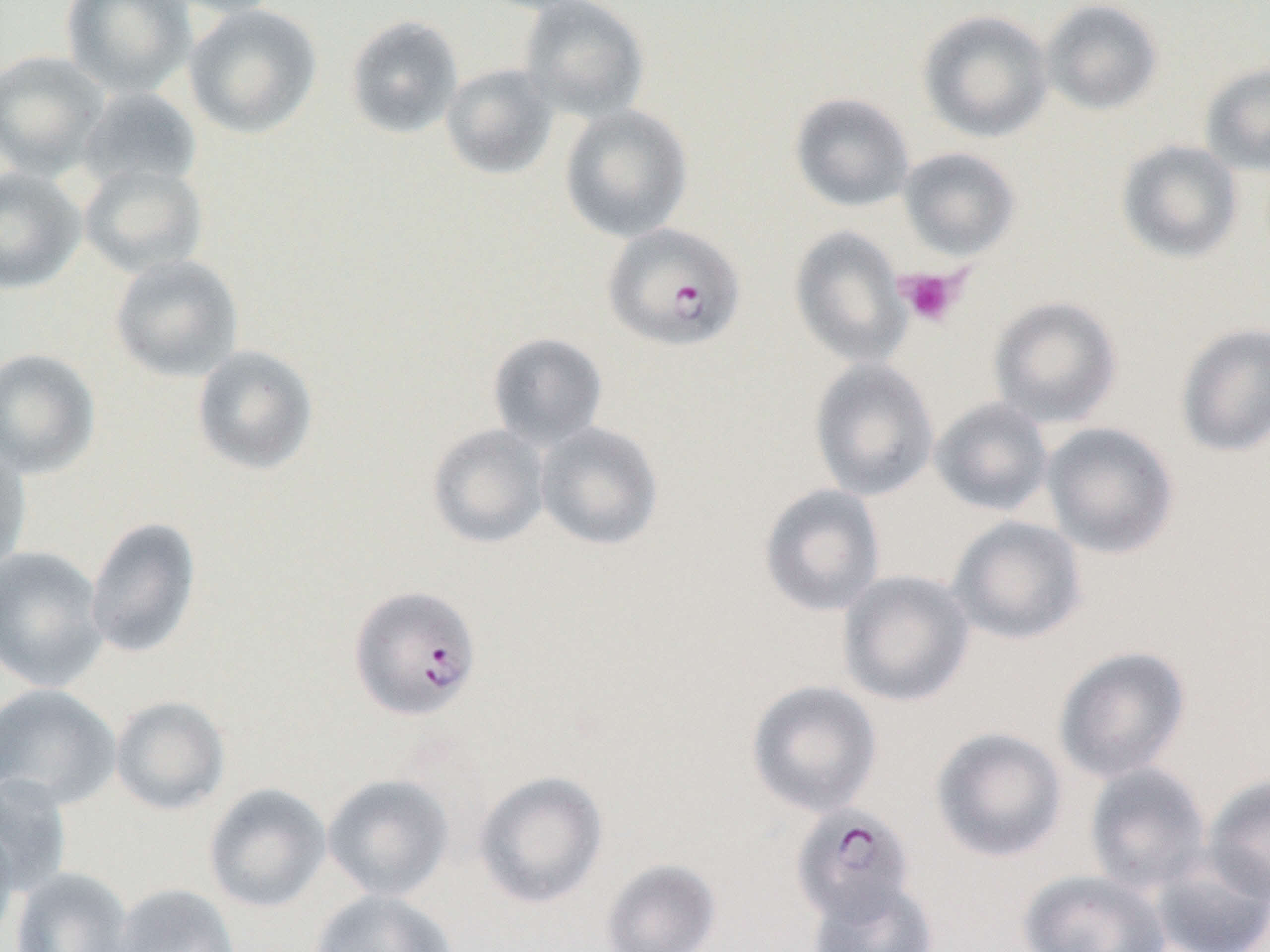
slide_level_diagnosis: Plasmodium falciparum
modality: light microscopy
magnification: 1000x
field_of_view: single
platelet_locations: 'approximate bounding boxes as [x1, y1, x2, y2] in pixels: [896, 267, 967, 327]'
uninfected_red_blood_cell_locations: 'approximate bounding boxes as [x1, y1, x2, y2] in pixels: [60, 0, 197, 98], [157, 0, 286, 18], [518, 0, 650, 122], [1041, 0, 1164, 116], [183, 4, 323, 139], [917, 9, 1053, 143], [345, 15, 464, 139], [0, 50, 110, 179], [1200, 63, 1270, 176], [441, 64, 559, 179], [78, 86, 202, 194], [789, 93, 915, 212], [559, 104, 693, 243], [1116, 139, 1244, 263], [897, 147, 1021, 261], [79, 162, 208, 278], [0, 167, 86, 294], [788, 226, 910, 367], [110, 254, 244, 382], [988, 296, 1122, 428], [1175, 323, 1270, 458], [487, 332, 609, 449], [191, 344, 319, 475], [0, 348, 101, 479], [809, 358, 940, 501], [929, 397, 1054, 517], [534, 421, 664, 551], [1041, 422, 1180, 559], [427, 423, 550, 549], [0, 442, 32, 577], [758, 483, 886, 617], [947, 515, 1088, 646], [85, 516, 202, 660], [0, 546, 108, 692], [837, 570, 975, 708], [1053, 645, 1192, 783], [746, 679, 883, 818], [0, 683, 122, 810], [110, 695, 231, 816], [930, 726, 1068, 862], [1084, 762, 1212, 895], [473, 770, 609, 909], [322, 774, 454, 902], [0, 775, 73, 896], [1203, 775, 1270, 905], [204, 783, 332, 913], [0, 822, 20, 946], [1149, 847, 1270, 952], [600, 859, 722, 952], [10, 867, 135, 952], [1019, 869, 1171, 952], [807, 878, 938, 952], [112, 883, 241, 952], [309, 889, 458, 952]'
preparation: thin blood smear
image_size: 1270×952 pixels
plasmodium_falciparum_infected_red_blood_cell_locations: 'approximate bounding boxes as [x1, y1, x2, y2] in pixels: [603, 222, 746, 352], [348, 585, 482, 721], [790, 802, 917, 926]'